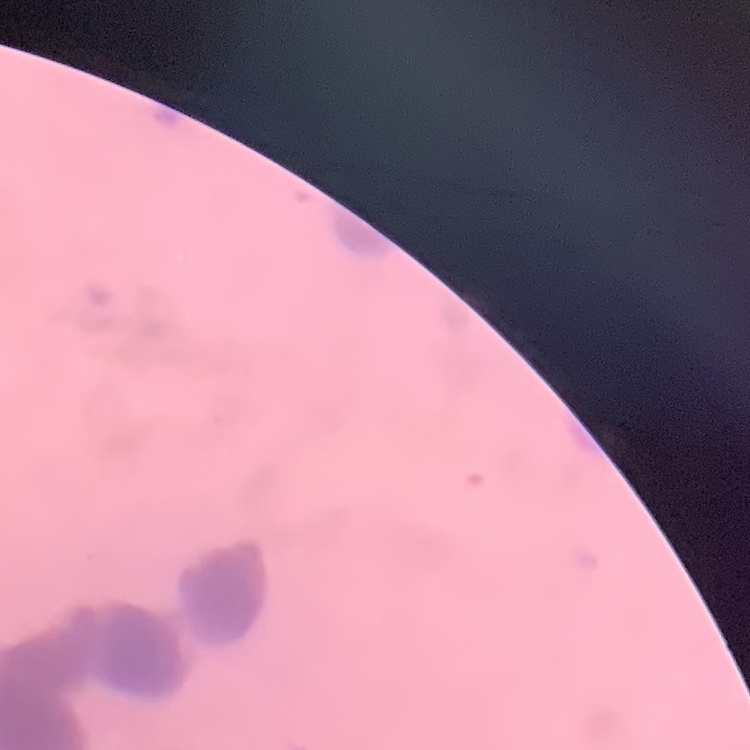

The erythrocytes show rouleaux formation. Thin peripheral smear. Field's or Giemsa stain. One tile cut from a larger photomicrograph.